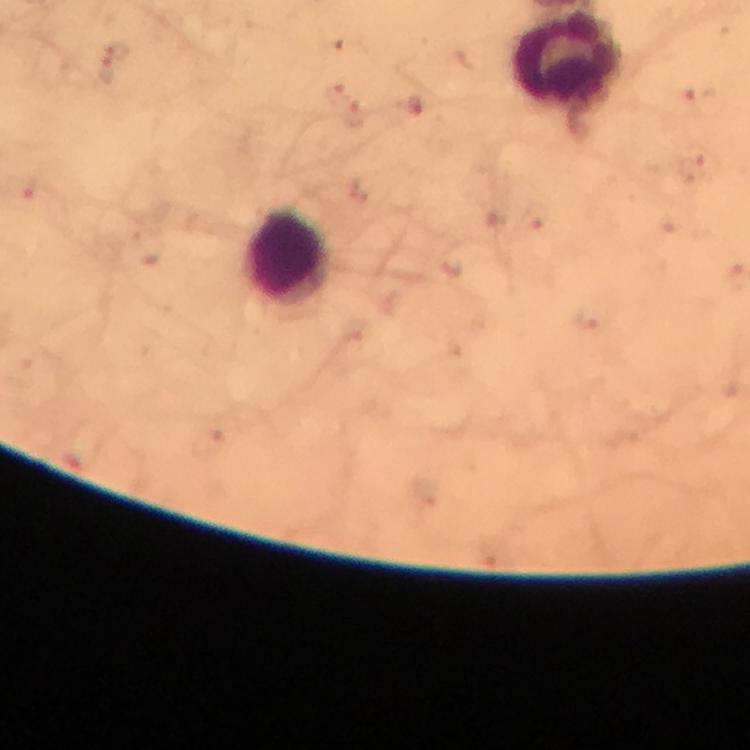
preparation = thick blood smear
Plasmodium parasite locations = approximate centers as (x, y) in pixels: (119, 48), (106, 71), (415, 106)
immersion oil = used
image size = 750×750 pixels
stain = Giemsa
magnification = 100x
context = from a malaria diagnostic workup
leukocyte locations = approximate centers as (x, y) in pixels: (567, 58), (288, 257)
capture = smartphone camera through the microscope
cropped from = a single field of view